Locate platelets.
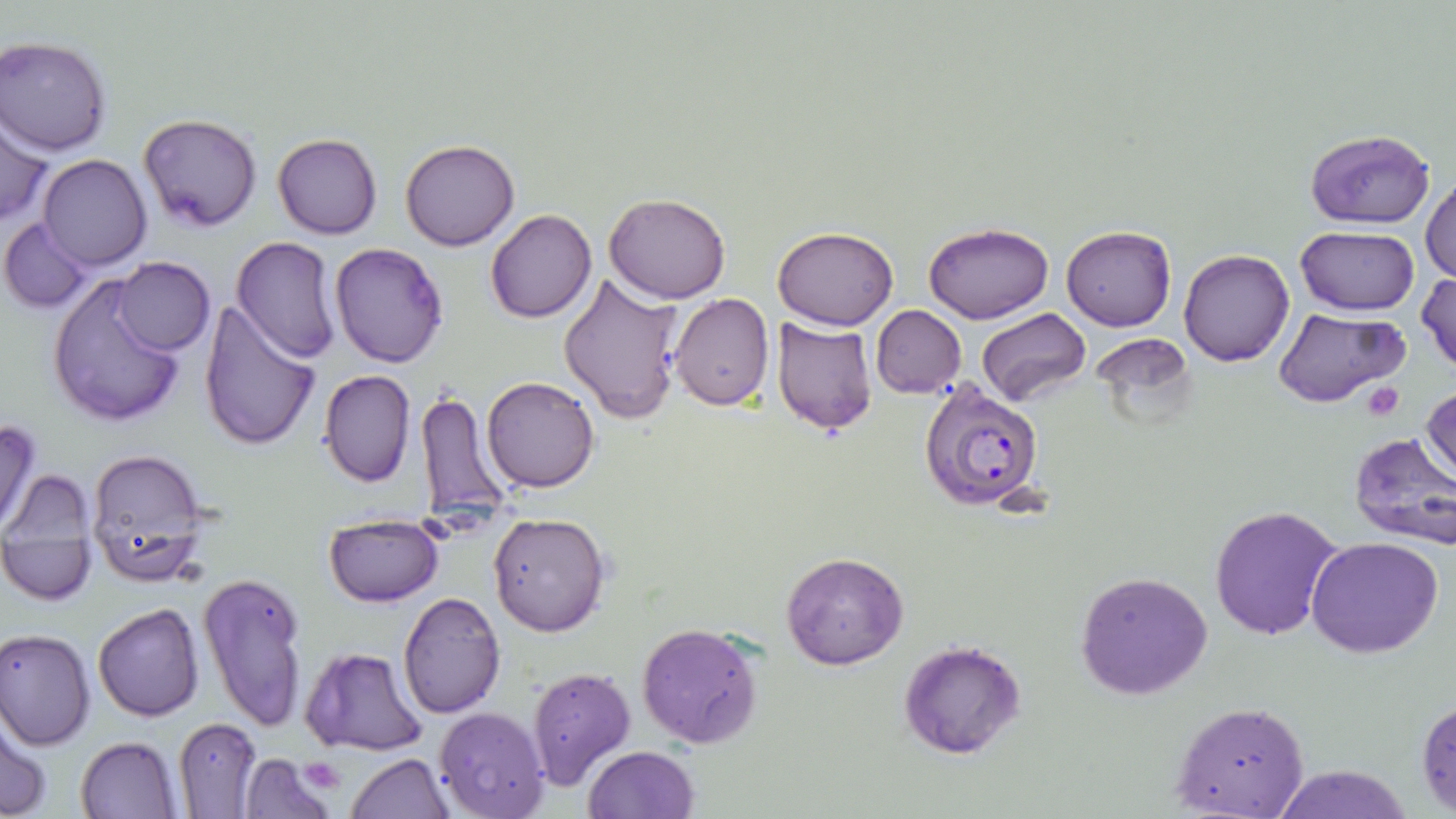
Approximate bounding boxes as [x1, y1, x2, y2] in pixels.
Platelets: [1360, 382, 1405, 420], [298, 757, 346, 793].

Plasmodium falciparum-infected red blood cell locations = approximate bounding boxes as [x1, y1, x2, y2] in pixels: [917, 383, 1045, 513]
slide-level diagnosis = Plasmodium falciparum
stain = May-Grünwald-Giemsa
field of view = single
image size = 1456×819 pixels
uninfected red blood cell locations = approximate bounding boxes as [x1, y1, x2, y2] in pixels: [1, 33, 116, 157], [138, 113, 262, 232], [1, 114, 50, 228], [1303, 127, 1435, 229], [273, 134, 382, 239], [401, 138, 518, 252], [38, 154, 152, 271], [1421, 170, 1455, 287], [603, 192, 731, 304], [486, 210, 596, 324], [1, 216, 94, 313], [924, 222, 1052, 324], [1062, 225, 1176, 332], [772, 226, 899, 330], [1295, 227, 1420, 314], [232, 236, 341, 363], [331, 244, 448, 369], [1178, 248, 1293, 366], [112, 256, 214, 356], [1416, 270, 1456, 376], [47, 272, 192, 429], [559, 272, 685, 422], [669, 292, 774, 410], [197, 299, 322, 454], [871, 305, 966, 397], [1275, 306, 1405, 408], [978, 307, 1091, 405], [771, 318, 877, 436], [318, 369, 416, 487], [483, 376, 599, 493], [1421, 379, 1456, 490], [414, 388, 515, 528], [0, 417, 43, 536], [1347, 432, 1456, 555], [85, 447, 212, 587], [0, 472, 102, 608], [1208, 503, 1343, 641], [489, 512, 610, 636], [323, 514, 444, 605], [1305, 537, 1444, 659], [780, 551, 908, 670], [198, 569, 311, 733], [1076, 570, 1213, 701], [398, 591, 505, 718], [93, 602, 205, 721], [636, 623, 764, 749], [0, 627, 97, 749], [899, 640, 1024, 758], [300, 644, 430, 758], [526, 665, 636, 791], [1416, 698, 1456, 814], [1170, 701, 1309, 818], [434, 708, 551, 819], [173, 717, 262, 817], [1, 719, 51, 819], [75, 735, 182, 818], [582, 745, 699, 819], [348, 754, 452, 818], [239, 755, 337, 818], [1270, 765, 1410, 819]
modality = optical microscopy
magnification = 1000x
preparation = thin blood smear